Classify this cell by malaria status.
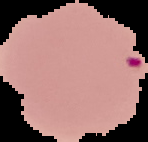

Uninfected.

preparation = thin blood film
image type = segmented cell region on a black background
image size = 148×142 pixels